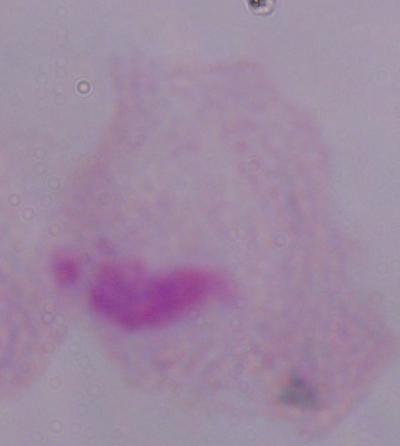

Summary:
  - Identification: trichomonad
  - Magnification: 1000x
  - Modality: micrograph